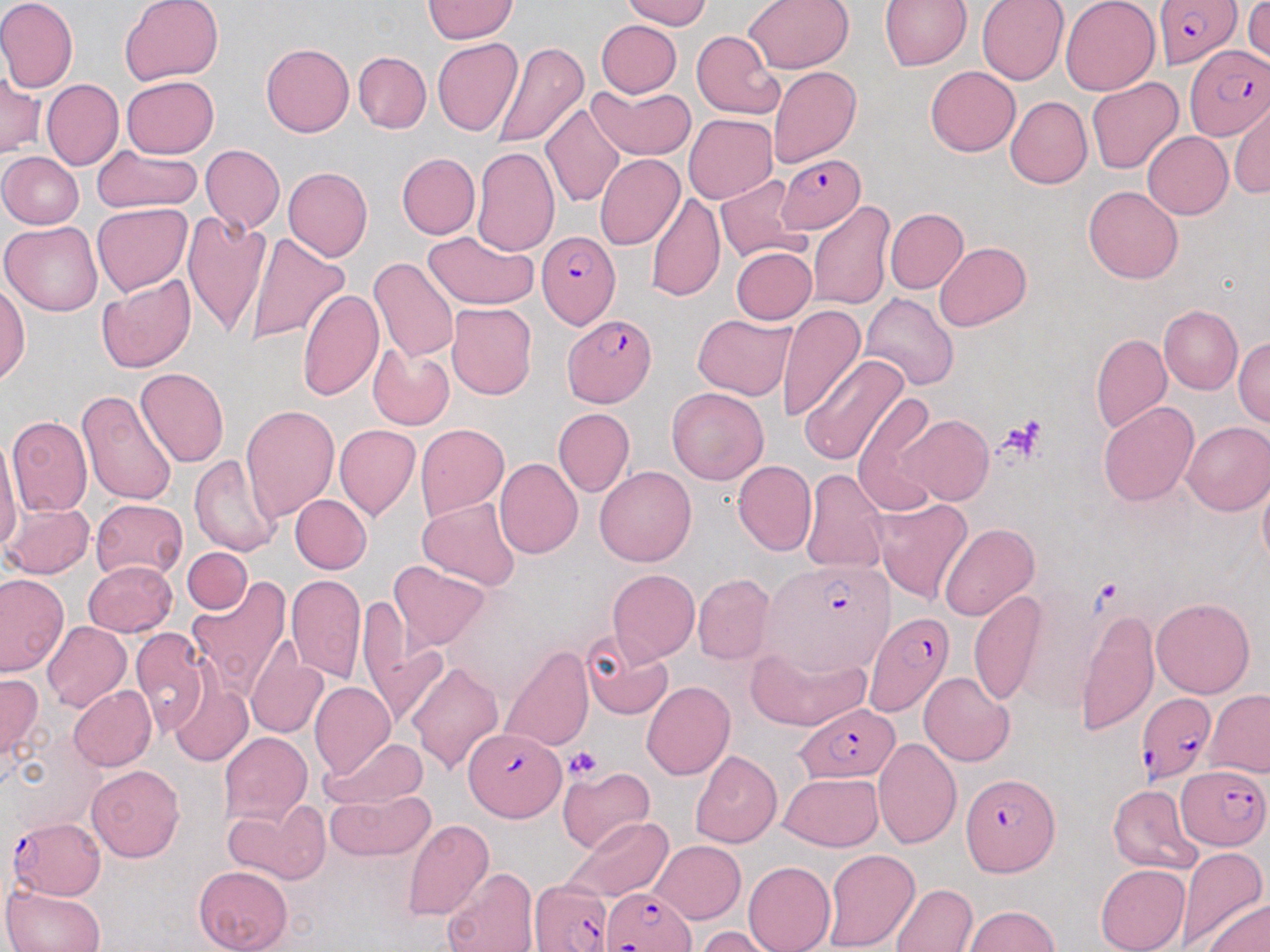
Summary:
  - Coordinate format: approximate bounding boxes as named x1/y1/x2/y2 corners in pixels
  - Plasmodium falciparum-infected red blood cell locations: (x1=1155, y1=3, x2=1246, y2=73), (x1=1186, y1=44, x2=1269, y2=140), (x1=778, y1=155, x2=866, y2=233), (x1=535, y1=230, x2=620, y2=331), (x1=563, y1=314, x2=656, y2=406), (x1=767, y1=558, x2=892, y2=676), (x1=864, y1=610, x2=953, y2=716), (x1=1137, y1=692, x2=1217, y2=784), (x1=796, y1=702, x2=902, y2=783), (x1=462, y1=728, x2=566, y2=824), (x1=1177, y1=766, x2=1270, y2=850), (x1=961, y1=772, x2=1060, y2=875), (x1=6, y1=816, x2=104, y2=898), (x1=529, y1=878, x2=613, y2=952), (x1=602, y1=886, x2=694, y2=952)
  - Platelet locations: (x1=999, y1=414, x2=1049, y2=462), (x1=565, y1=745, x2=603, y2=780)
  - Uninfected red blood cell locations: (x1=0, y1=0, x2=78, y2=93), (x1=119, y1=0, x2=223, y2=87), (x1=623, y1=0, x2=712, y2=30), (x1=744, y1=0, x2=854, y2=73), (x1=880, y1=0, x2=971, y2=72), (x1=978, y1=0, x2=1068, y2=85), (x1=1060, y1=0, x2=1160, y2=96), (x1=423, y1=1, x2=516, y2=43), (x1=1245, y1=2, x2=1270, y2=64), (x1=596, y1=19, x2=682, y2=97), (x1=692, y1=30, x2=784, y2=119), (x1=433, y1=38, x2=523, y2=137), (x1=492, y1=40, x2=589, y2=152), (x1=260, y1=43, x2=354, y2=137), (x1=353, y1=51, x2=431, y2=133), (x1=925, y1=65, x2=1019, y2=156), (x1=769, y1=66, x2=860, y2=166), (x1=0, y1=73, x2=44, y2=159), (x1=122, y1=75, x2=219, y2=159), (x1=1087, y1=78, x2=1183, y2=174), (x1=42, y1=80, x2=124, y2=170), (x1=504, y1=80, x2=599, y2=205), (x1=589, y1=83, x2=696, y2=161), (x1=1005, y1=96, x2=1092, y2=188), (x1=1230, y1=99, x2=1270, y2=201), (x1=541, y1=103, x2=624, y2=208), (x1=685, y1=114, x2=777, y2=204), (x1=1142, y1=131, x2=1232, y2=218), (x1=93, y1=144, x2=201, y2=214), (x1=200, y1=144, x2=284, y2=233), (x1=472, y1=147, x2=558, y2=255), (x1=0, y1=151, x2=84, y2=229), (x1=397, y1=153, x2=480, y2=238), (x1=596, y1=154, x2=684, y2=250), (x1=283, y1=167, x2=373, y2=262), (x1=715, y1=174, x2=809, y2=263), (x1=1083, y1=186, x2=1184, y2=284), (x1=646, y1=192, x2=726, y2=302), (x1=808, y1=201, x2=897, y2=312), (x1=92, y1=203, x2=191, y2=296), (x1=884, y1=209, x2=968, y2=293), (x1=182, y1=211, x2=272, y2=340), (x1=1, y1=220, x2=104, y2=316), (x1=243, y1=230, x2=349, y2=346), (x1=422, y1=230, x2=539, y2=309), (x1=934, y1=242, x2=1030, y2=330), (x1=731, y1=246, x2=816, y2=324), (x1=369, y1=256, x2=459, y2=362), (x1=96, y1=275, x2=197, y2=374), (x1=0, y1=284, x2=30, y2=384), (x1=296, y1=288, x2=382, y2=402), (x1=860, y1=293, x2=960, y2=393), (x1=446, y1=302, x2=537, y2=400), (x1=776, y1=304, x2=865, y2=421), (x1=1158, y1=305, x2=1243, y2=395), (x1=693, y1=314, x2=797, y2=400), (x1=1091, y1=333, x2=1171, y2=434), (x1=1234, y1=337, x2=1269, y2=429), (x1=367, y1=345, x2=454, y2=429), (x1=797, y1=353, x2=910, y2=466), (x1=135, y1=368, x2=228, y2=467), (x1=667, y1=388, x2=769, y2=485), (x1=75, y1=389, x2=176, y2=506), (x1=852, y1=393, x2=943, y2=514), (x1=1098, y1=401, x2=1199, y2=506), (x1=240, y1=404, x2=340, y2=523), (x1=552, y1=407, x2=635, y2=497), (x1=897, y1=414, x2=994, y2=505), (x1=7, y1=416, x2=92, y2=515), (x1=1182, y1=422, x2=1270, y2=515), (x1=415, y1=423, x2=509, y2=520), (x1=334, y1=425, x2=420, y2=521), (x1=0, y1=434, x2=23, y2=559), (x1=189, y1=455, x2=282, y2=556), (x1=494, y1=458, x2=582, y2=558), (x1=732, y1=461, x2=816, y2=556), (x1=594, y1=465, x2=696, y2=567), (x1=801, y1=468, x2=888, y2=574), (x1=1258, y1=472, x2=1270, y2=575), (x1=289, y1=495, x2=371, y2=574), (x1=417, y1=497, x2=521, y2=591), (x1=871, y1=498, x2=972, y2=603), (x1=90, y1=499, x2=188, y2=579), (x1=2, y1=502, x2=94, y2=579), (x1=939, y1=523, x2=1039, y2=622), (x1=182, y1=548, x2=252, y2=614), (x1=85, y1=561, x2=176, y2=637), (x1=389, y1=561, x2=490, y2=651), (x1=607, y1=568, x2=700, y2=664), (x1=0, y1=572, x2=67, y2=677), (x1=285, y1=573, x2=367, y2=684), (x1=693, y1=573, x2=774, y2=665), (x1=187, y1=576, x2=293, y2=694), (x1=1010, y1=586, x2=1104, y2=717), (x1=968, y1=588, x2=1047, y2=706), (x1=1150, y1=597, x2=1255, y2=698), (x1=355, y1=598, x2=442, y2=727), (x1=1076, y1=607, x2=1158, y2=738), (x1=42, y1=622, x2=130, y2=712), (x1=128, y1=627, x2=211, y2=736), (x1=580, y1=633, x2=674, y2=720), (x1=746, y1=643, x2=872, y2=731), (x1=246, y1=645, x2=328, y2=739), (x1=499, y1=645, x2=594, y2=753), (x1=406, y1=661, x2=503, y2=776), (x1=919, y1=671, x2=1015, y2=767), (x1=0, y1=672, x2=43, y2=768), (x1=167, y1=678, x2=253, y2=767), (x1=641, y1=681, x2=735, y2=781), (x1=310, y1=683, x2=394, y2=777), (x1=69, y1=686, x2=158, y2=771), (x1=1204, y1=690, x2=1269, y2=778), (x1=218, y1=732, x2=311, y2=825), (x1=318, y1=736, x2=431, y2=811), (x1=873, y1=737, x2=961, y2=849), (x1=690, y1=750, x2=782, y2=848), (x1=86, y1=765, x2=185, y2=861), (x1=557, y1=767, x2=655, y2=853), (x1=778, y1=774, x2=884, y2=852), (x1=1108, y1=783, x2=1203, y2=876), (x1=323, y1=791, x2=434, y2=861), (x1=226, y1=799, x2=331, y2=884), (x1=562, y1=816, x2=674, y2=901), (x1=402, y1=819, x2=494, y2=921), (x1=651, y1=840, x2=746, y2=924), (x1=1175, y1=847, x2=1266, y2=950), (x1=821, y1=849, x2=919, y2=952), (x1=743, y1=861, x2=835, y2=952), (x1=194, y1=865, x2=293, y2=952), (x1=1095, y1=865, x2=1190, y2=952), (x1=440, y1=868, x2=537, y2=952), (x1=2, y1=883, x2=105, y2=952), (x1=890, y1=883, x2=977, y2=952), (x1=1201, y1=897, x2=1269, y2=952), (x1=962, y1=905, x2=1061, y2=951), (x1=695, y1=926, x2=780, y2=952)
  - Slide-level diagnosis: Plasmodium falciparum
  - Magnification: 1000x
  - Field of view: single
  - Image size: 1270×952 pixels
  - Preparation: thin blood film
  - Modality: light microscopy
  - Stain: May-Grünwald-Giemsa